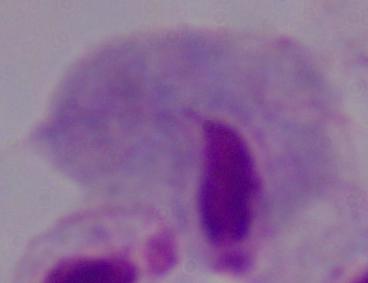

modality = photomicrograph
magnification = 1000x
identification = trichomonad